Describe the morphology of the erythrocytes.
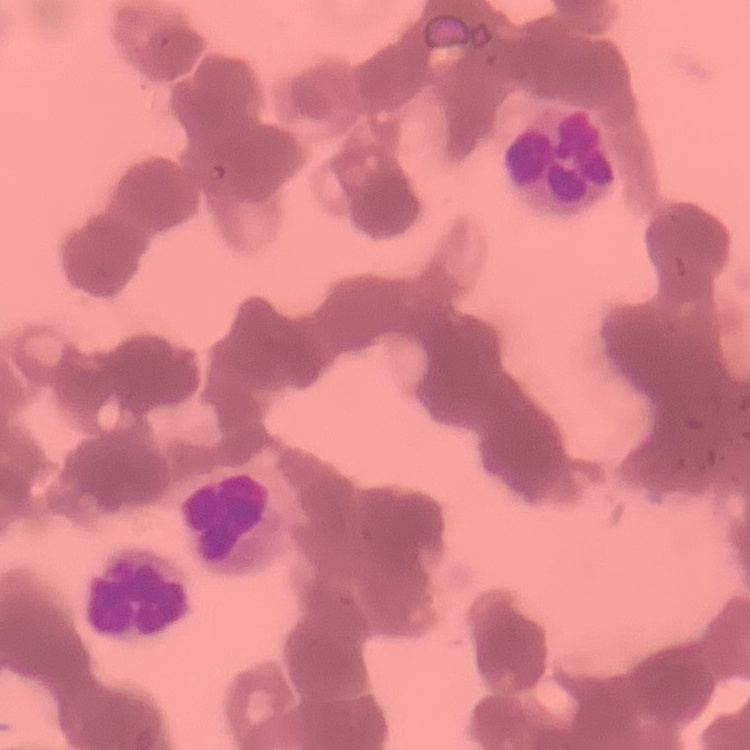
They show rouleaux formation.

Summary:
  - Preparation: thin blood film
  - Stain: Field's or Giemsa
  - Image type: square crop of a larger photomicrograph